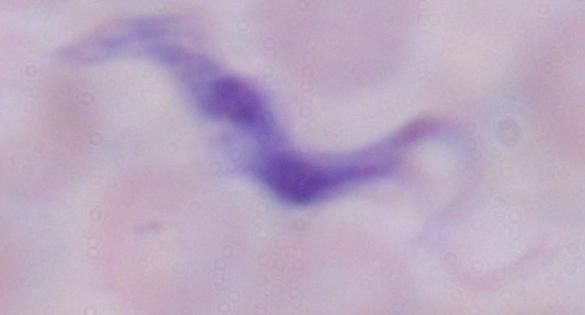 Micrograph. Captured at 1000x magnification. A trypanosome is shown.